Assess the morphology of the erythrocytes.
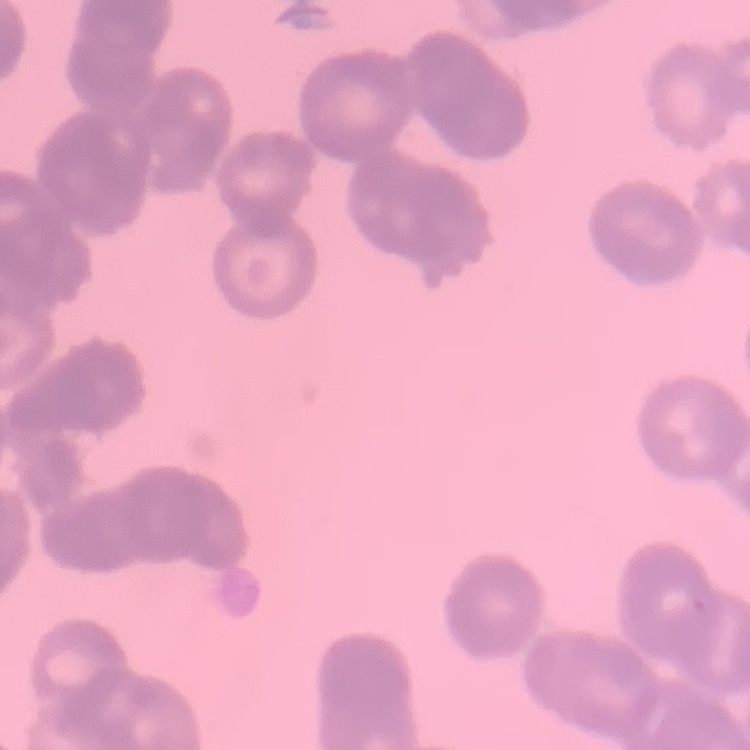

Rouleaux formation.

Summary:
  - Image type: one tile cut from a larger photomicrograph
  - Preparation: thin blood smear
  - Stain: Field's or Giemsa